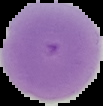
Segmented cell region on a black background. From a thin blood smear. Result: no malaria parasites seen. Image is 103×106 pixels.